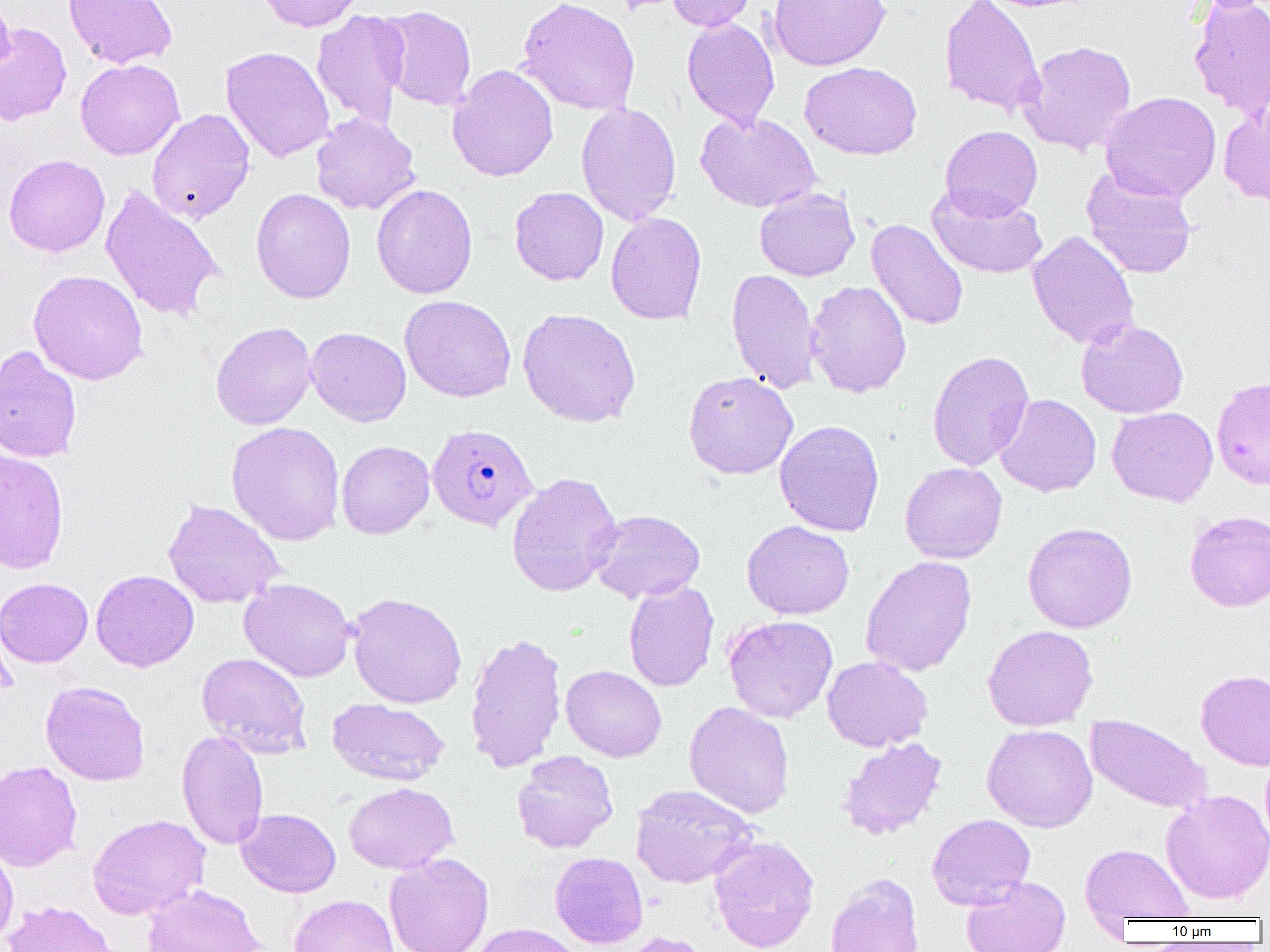

slide-level diagnosis = Plasmodium falciparum
magnification = 1000x
field of view = one of a larger specimen
preparation = thin blood film
Plasmodium falciparum-infected red blood cell locations = approximate bounding boxes as (x1, y1, x2, y2) in pixels: (427, 424, 538, 532)
image size = 1270×952 pixels
uninfected red blood cell locations = approximate bounding boxes as (x1, y1, x2, y2) in pixels: (0, 0, 16, 80), (63, 0, 178, 69), (257, 0, 366, 32), (517, 0, 640, 116), (667, 0, 757, 32), (768, 0, 890, 71), (939, 0, 1045, 119), (1187, 0, 1270, 119), (378, 5, 477, 111), (311, 10, 410, 130), (682, 17, 780, 129), (0, 21, 72, 126), (1018, 40, 1137, 156), (221, 46, 335, 163), (75, 59, 185, 160), (799, 61, 922, 159), (447, 64, 558, 181), (1100, 91, 1222, 203), (1218, 96, 1270, 207), (576, 101, 682, 225), (146, 108, 255, 224), (695, 112, 820, 212), (310, 113, 421, 215), (940, 125, 1043, 220), (3, 154, 110, 257), (1081, 166, 1199, 279), (371, 184, 478, 299), (926, 184, 1049, 279), (99, 185, 225, 323), (509, 187, 609, 285), (251, 188, 356, 304), (754, 188, 860, 281), (606, 211, 707, 325), (866, 219, 968, 331), (1027, 230, 1140, 350), (726, 268, 822, 394), (28, 269, 148, 385), (805, 280, 912, 397), (400, 295, 516, 402), (517, 308, 641, 428), (1075, 318, 1189, 419), (210, 321, 317, 429), (305, 327, 411, 427), (0, 344, 83, 463), (927, 350, 1034, 471), (683, 371, 798, 479), (1211, 374, 1270, 490), (994, 393, 1102, 497), (1107, 407, 1218, 507), (774, 420, 885, 537), (225, 421, 346, 546), (336, 440, 434, 539), (0, 449, 69, 575), (900, 462, 1007, 564), (506, 471, 623, 597), (162, 499, 285, 609), (588, 509, 706, 603), (1184, 510, 1270, 611), (741, 520, 855, 620), (1022, 521, 1137, 633), (860, 555, 977, 676), (91, 569, 199, 672), (0, 577, 93, 667), (239, 577, 356, 682), (623, 580, 720, 692), (346, 592, 467, 709), (723, 614, 838, 722), (982, 624, 1098, 731), (464, 631, 567, 773), (196, 652, 312, 758), (821, 656, 933, 752), (561, 665, 666, 761), (1195, 668, 1270, 770), (40, 681, 150, 785), (327, 698, 449, 785), (684, 701, 795, 818), (1085, 713, 1212, 814), (982, 724, 1097, 832), (176, 730, 269, 850), (838, 737, 948, 839), (1260, 747, 1270, 852), (511, 750, 618, 853), (0, 760, 83, 872), (344, 782, 457, 874), (631, 784, 757, 888), (1160, 789, 1270, 904), (237, 808, 341, 897), (87, 814, 210, 920), (926, 814, 1035, 910), (709, 835, 820, 952), (0, 841, 18, 949), (1079, 843, 1194, 921), (549, 851, 648, 949), (384, 853, 494, 952), (826, 872, 924, 952), (961, 875, 1071, 952), (141, 883, 264, 952), (289, 894, 399, 952), (3, 900, 118, 952), (469, 922, 584, 952), (615, 931, 711, 952)
modality = light microscopy